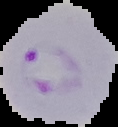
image size = 118×127 pixels
image type = segmented cell region with the area outside set to black
malaria status = parasitized
preparation = thin blood film